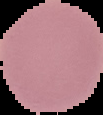

Malaria status: uninfected. From a thin blood smear. Image is 103×115 pixels. Segmented cell region on a black background.